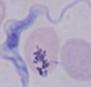

identification: trypanosome
modality: micrograph
magnification: 1000x